Identify the blood parasite species.
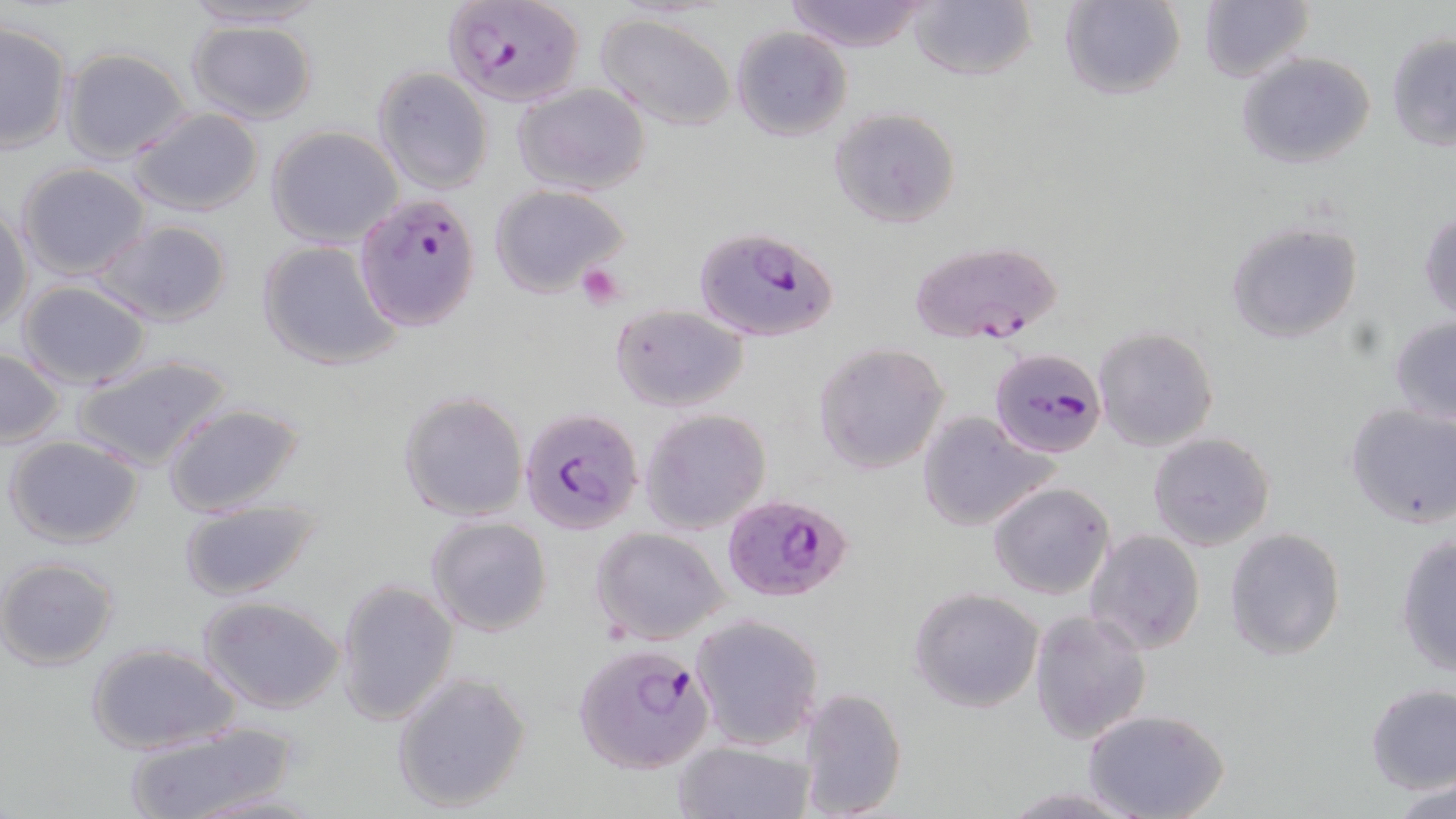
Plasmodium falciparum.

modality = light microscopy
stain = May-Grünwald-Giemsa
preparation = thin blood film
uninfected red blood cell locations = approximate bounding boxes as named x1/y1/x2/y2 corners in pixels: (x1=176, y1=0, x2=332, y2=30), (x1=784, y1=0, x2=929, y2=52), (x1=1057, y1=0, x2=1187, y2=101), (x1=909, y1=1, x2=1035, y2=81), (x1=1196, y1=2, x2=1315, y2=83), (x1=594, y1=12, x2=738, y2=132), (x1=186, y1=19, x2=320, y2=126), (x1=0, y1=22, x2=73, y2=155), (x1=730, y1=26, x2=852, y2=141), (x1=1385, y1=32, x2=1456, y2=152), (x1=60, y1=47, x2=193, y2=165), (x1=1235, y1=52, x2=1377, y2=170), (x1=372, y1=67, x2=495, y2=193), (x1=512, y1=82, x2=652, y2=197), (x1=829, y1=107, x2=960, y2=228), (x1=130, y1=108, x2=263, y2=217), (x1=266, y1=125, x2=404, y2=247), (x1=15, y1=162, x2=150, y2=280), (x1=489, y1=184, x2=630, y2=298), (x1=0, y1=204, x2=32, y2=334), (x1=1419, y1=209, x2=1455, y2=324), (x1=96, y1=218, x2=232, y2=327), (x1=1225, y1=218, x2=1361, y2=344), (x1=257, y1=238, x2=403, y2=371), (x1=16, y1=279, x2=153, y2=388), (x1=609, y1=305, x2=748, y2=413), (x1=1388, y1=314, x2=1456, y2=426), (x1=1093, y1=325, x2=1219, y2=451), (x1=814, y1=342, x2=952, y2=474), (x1=1, y1=347, x2=65, y2=446), (x1=71, y1=352, x2=233, y2=471), (x1=397, y1=390, x2=528, y2=522), (x1=163, y1=401, x2=306, y2=517), (x1=1344, y1=401, x2=1456, y2=528), (x1=640, y1=408, x2=771, y2=535), (x1=915, y1=409, x2=1058, y2=533), (x1=1147, y1=430, x2=1275, y2=551), (x1=5, y1=436, x2=145, y2=548), (x1=988, y1=482, x2=1115, y2=601), (x1=174, y1=499, x2=319, y2=602), (x1=425, y1=515, x2=552, y2=637), (x1=591, y1=527, x2=730, y2=646), (x1=1224, y1=527, x2=1346, y2=661), (x1=1085, y1=528, x2=1206, y2=654), (x1=1394, y1=530, x2=1455, y2=677), (x1=0, y1=557, x2=121, y2=671), (x1=334, y1=577, x2=460, y2=727), (x1=909, y1=588, x2=1045, y2=712), (x1=200, y1=598, x2=344, y2=715), (x1=1028, y1=609, x2=1152, y2=744), (x1=689, y1=613, x2=825, y2=751), (x1=85, y1=642, x2=240, y2=754), (x1=391, y1=671, x2=532, y2=815), (x1=1365, y1=684, x2=1456, y2=795), (x1=794, y1=687, x2=908, y2=819), (x1=1083, y1=709, x2=1229, y2=819), (x1=120, y1=716, x2=302, y2=819), (x1=675, y1=740, x2=815, y2=819), (x1=1389, y1=778, x2=1456, y2=819), (x1=994, y1=787, x2=1142, y2=818)
magnification = 1000x
image size = 1456×819 pixels
Plasmodium falciparum-infected red blood cell locations = approximate bounding boxes as named x1/y1/x2/y2 corners in pixels: (x1=442, y1=0, x2=586, y2=106), (x1=345, y1=193, x2=479, y2=335), (x1=694, y1=225, x2=840, y2=341), (x1=905, y1=238, x2=1064, y2=347), (x1=987, y1=350, x2=1103, y2=463), (x1=518, y1=406, x2=646, y2=537), (x1=725, y1=492, x2=849, y2=600), (x1=572, y1=642, x2=717, y2=775)
platelet locations = approximate bounding boxes as named x1/y1/x2/y2 corners in pixels: (x1=576, y1=263, x2=627, y2=309)
field of view = one of a larger specimen